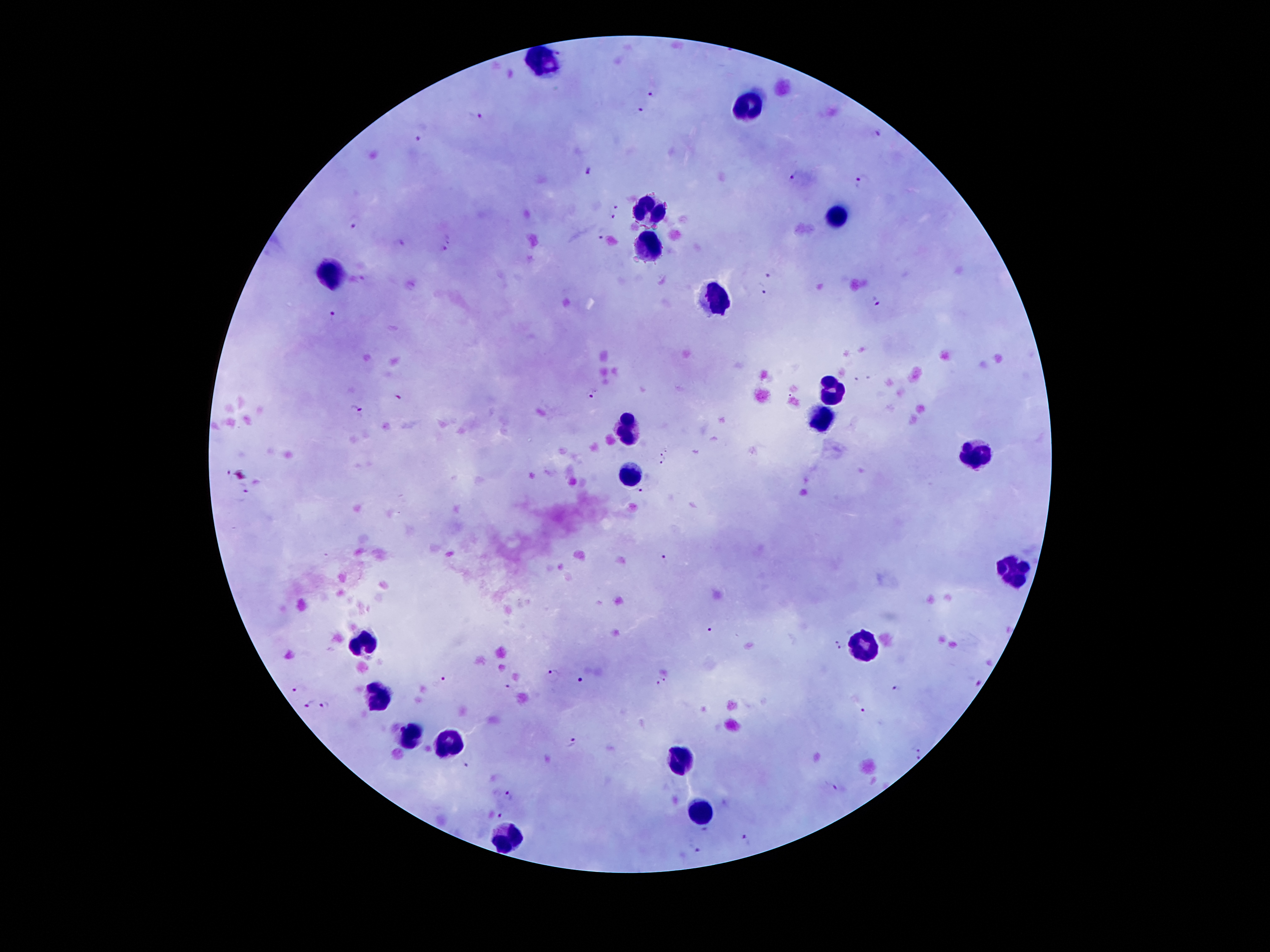 Approximate centers as (x, y) in pixels. Leukocyte locations: (543, 61), (748, 109), (651, 208), (837, 217), (650, 251), (331, 275), (716, 299), (830, 394), (819, 418), (627, 427), (973, 456), (630, 477), (1012, 571), (364, 641), (865, 643), (378, 695), (410, 738), (450, 741), (685, 760), (697, 814), (502, 839). Malaria parasite locations: (558, 51), (653, 90), (637, 110), (476, 115), (877, 135), (415, 141), (590, 170), (795, 176), (861, 180), (618, 205), (611, 218), (352, 223), (602, 232), (399, 244), (446, 244), (770, 272), (362, 279), (760, 288), (875, 303), (331, 314), (866, 375), (856, 380), (593, 391), (397, 396), (789, 397), (355, 410), (666, 450), (660, 456), (661, 463), (228, 470), (244, 487), (644, 490), (666, 558), (711, 630), (838, 639), (841, 649), (553, 674), (665, 677), (443, 678), (582, 679), (658, 685), (508, 687), (296, 689), (897, 689), (309, 704), (326, 705), (864, 710), (572, 742), (916, 747), (919, 757), (465, 763), (832, 787), (508, 795), (500, 816), (706, 830), (748, 842), (696, 849). One field from this slide. Patient malaria status: infected with Plasmodium falciparum. Thick blood smear. Image is 1270×952 pixels. Smartphone photograph taken through the microscope eyepiece. Giemsa-stained preparation. 100x magnification.